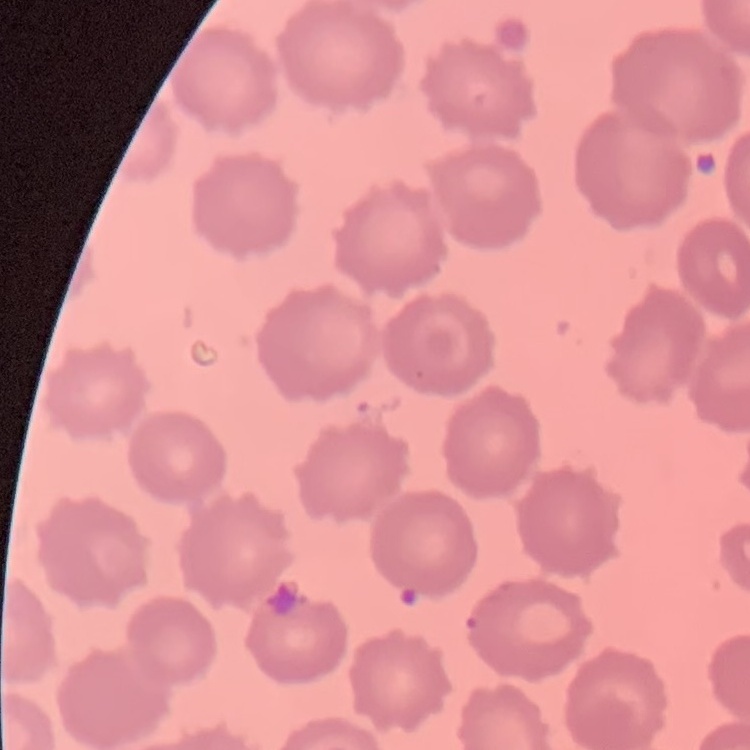 The erythrocytes show no rouleaux formation. Stained with either Field's or Giemsa. Square crop of a larger photomicrograph. Thin blood film.